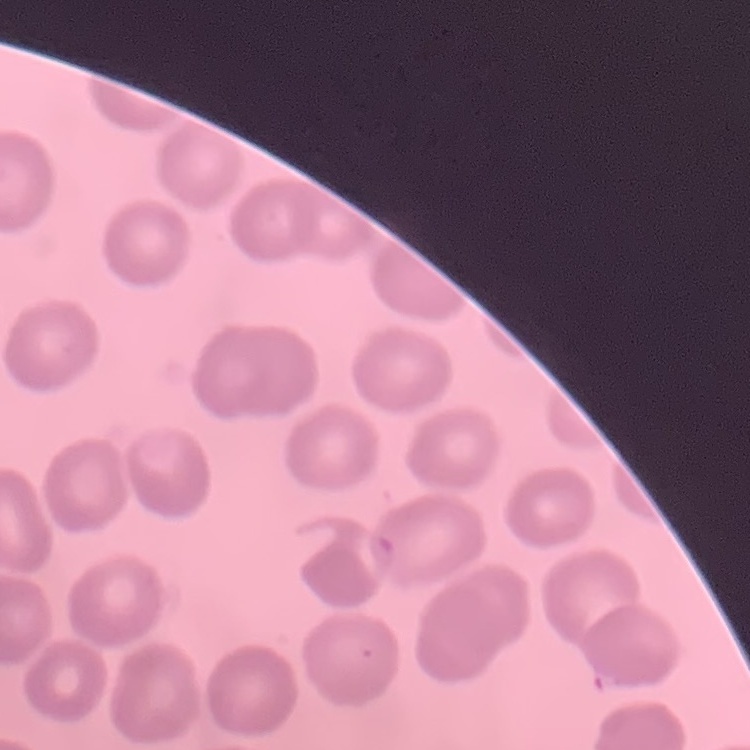
The red blood cells exhibit no rouleaux formation. Stained with either Field's or Giemsa. Thin blood film. One tile cut from a larger photomicrograph.